Assess this cell for malaria.
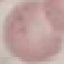

It is uninfected.

image_type: cell patch, automatically extracted from a larger field of view and resized to 64 × 64 pixels
preparation: thin blood film
stain: Giemsa
capture: smartphone camera at the microscope eyepiece